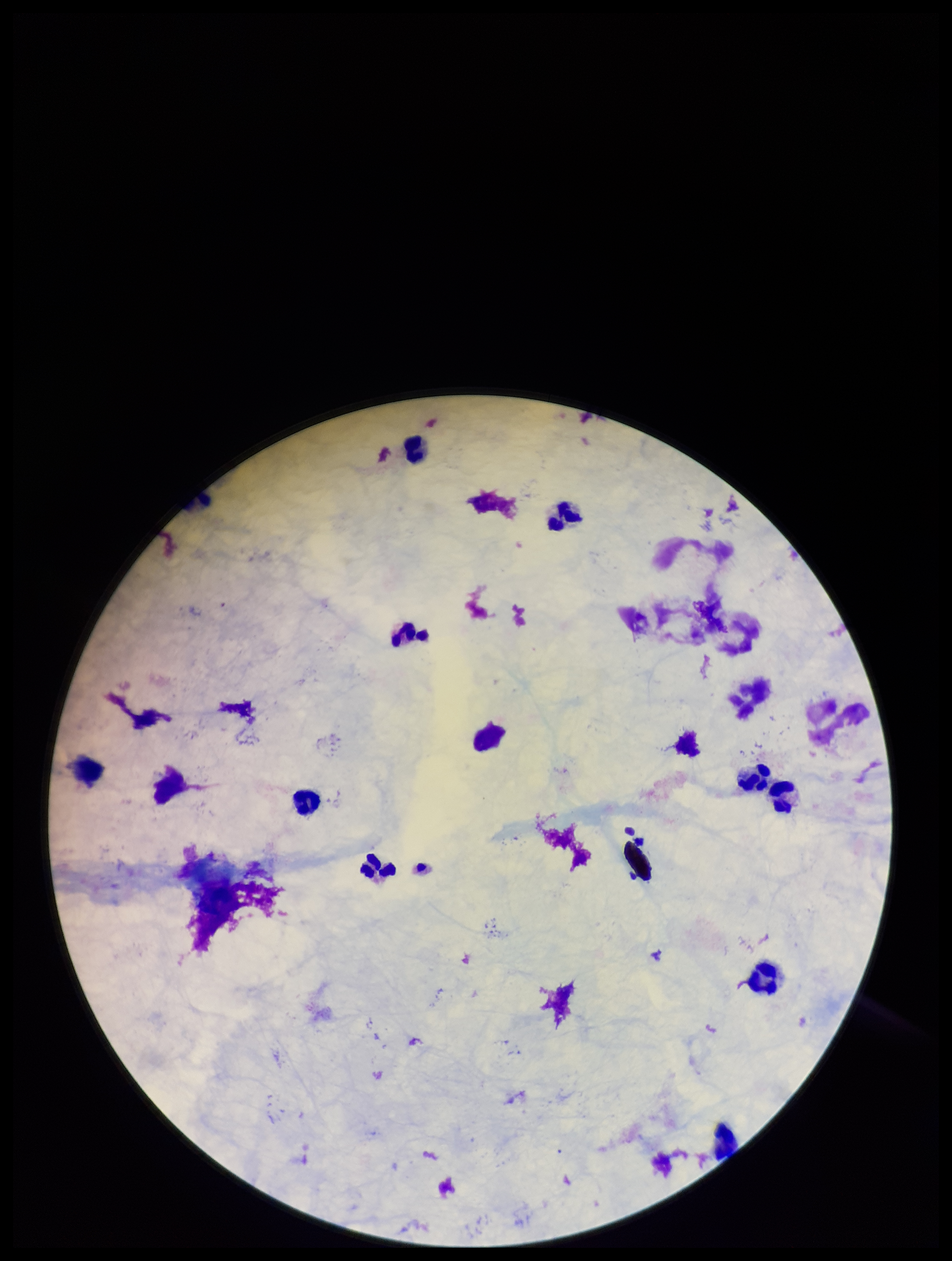

Stained with Giemsa. Parasite count: 0. Patient malaria status: negative. Leukocyte count: 12. Image is 952×1261 pixels. Plasmodium parasites: none identified. Preparation: thick. One field from this slide. Photographed through the microscope eyepiece with a smartphone camera.